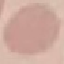
malaria status = uninfected
preparation = thin blood film
stain = Giemsa
capture = smartphone through the microscope eyepiece
image type = cell patch, automatically extracted from a larger field of view and resized to 64 × 64 pixels